Outline each uninfected red blood cell.
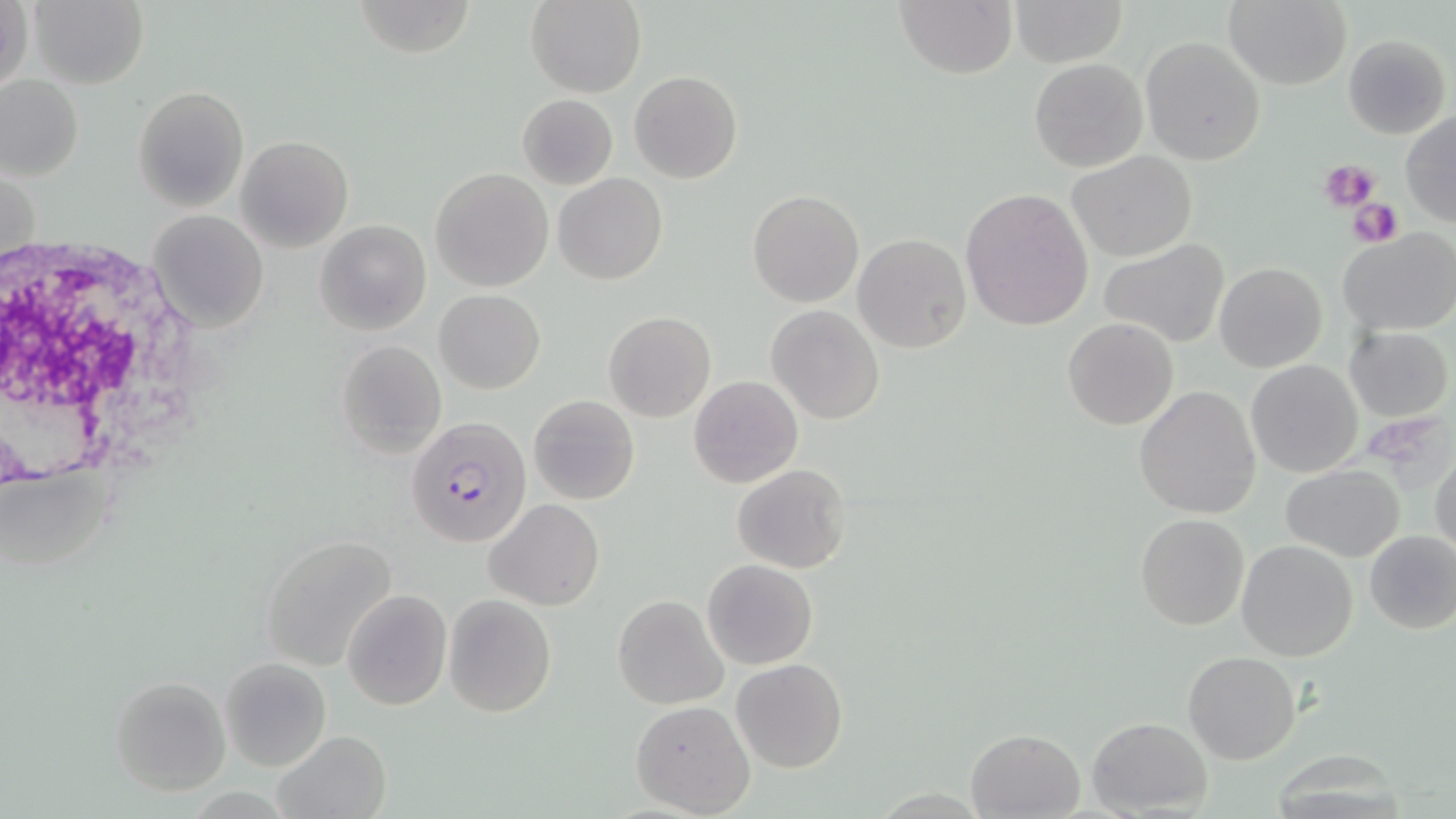

Approximate bounding boxes as (x1, y1, x2, y2) in pixels.
Uninfected red blood cells: (1, 0, 33, 97), (28, 0, 149, 88), (353, 0, 478, 57), (526, 0, 646, 98), (895, 0, 1017, 79), (1012, 0, 1125, 65), (1223, 1, 1351, 89), (1343, 34, 1449, 140), (1140, 36, 1266, 166), (1029, 57, 1147, 172), (629, 70, 743, 184), (1, 75, 83, 181), (133, 85, 248, 210), (517, 94, 618, 189), (1401, 110, 1456, 228), (237, 135, 354, 252), (1067, 149, 1198, 263), (431, 167, 553, 292), (553, 173, 669, 286), (960, 186, 1095, 332), (748, 190, 863, 307), (148, 210, 268, 333), (314, 219, 432, 336), (1338, 228, 1456, 335), (852, 234, 972, 355), (1098, 240, 1229, 348), (1213, 262, 1326, 372), (434, 289, 545, 394), (766, 305, 885, 425), (603, 312, 715, 423), (1063, 318, 1179, 431), (1345, 326, 1453, 421), (336, 339, 446, 458), (1247, 360, 1363, 477), (688, 375, 804, 488), (1134, 385, 1261, 520), (529, 394, 640, 506), (1430, 448, 1456, 559), (733, 464, 852, 575), (1280, 465, 1404, 562), (485, 500, 605, 609), (1136, 512, 1250, 630), (1364, 527, 1456, 634), (259, 533, 402, 671), (1236, 539, 1359, 660), (702, 559, 819, 669), (341, 589, 451, 711), (444, 593, 556, 716), (612, 594, 728, 709), (1183, 650, 1301, 765), (220, 658, 331, 770), (732, 658, 849, 772), (110, 675, 232, 795), (630, 699, 755, 818), (1086, 717, 1212, 816), (966, 727, 1086, 818), (274, 732, 391, 819).

slide_level_diagnosis: Plasmodium falciparum
field_of_view: one of a larger specimen
white_blood_cell_locations: 'approximate bounding boxes as (x1, y1, x2, y2) in pixels: (0, 228, 217, 495)'
image_size: 1456×819 pixels
magnification: 1000x
plasmodium_falciparum_infected_red_blood_cell_locations: 'approximate bounding boxes as (x1, y1, x2, y2) in pixels: (404, 414, 532, 550)'
modality: light microscopy
stain: May-Grünwald-Giemsa
preparation: thin blood smear
platelet_locations: 'approximate bounding boxes as (x1, y1, x2, y2) in pixels: (1320, 159, 1379, 212), (1348, 196, 1404, 248)'